Classify this cell by malaria status.
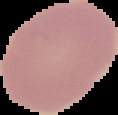

It is uninfected.

{
  "preparation": "thin blood smear",
  "image_type": "segmented cell region with the area outside set to black",
  "image_size": "118×115 pixels"
}